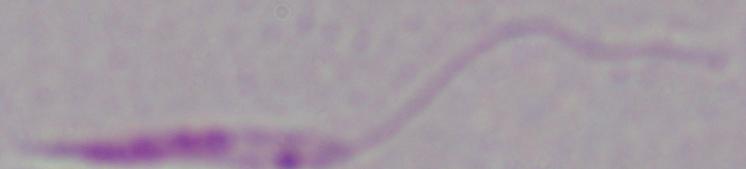
Summary:
  - Modality: photomicrograph
  - Magnification: 1000x
  - Identification: Leishmania